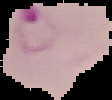
result = Plasmodium parasites detected
preparation = thin blood smear
image size = 112×100 pixels
image type = segmented cell region with the area outside set to black